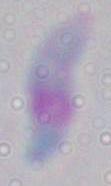

Photomicrograph. 1000x magnification. Toxoplasma gondii is seen.